Classify this cell by malaria status.
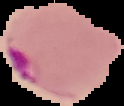
It is parasitized.

image_type: segmented cell region on a black background
preparation: thin blood film
image_size: 124×106 pixels